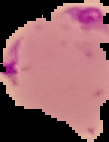

image size = 109×142 pixels
image type = segmented cell region on a black background
result = malaria parasites identified
preparation = thin blood smear